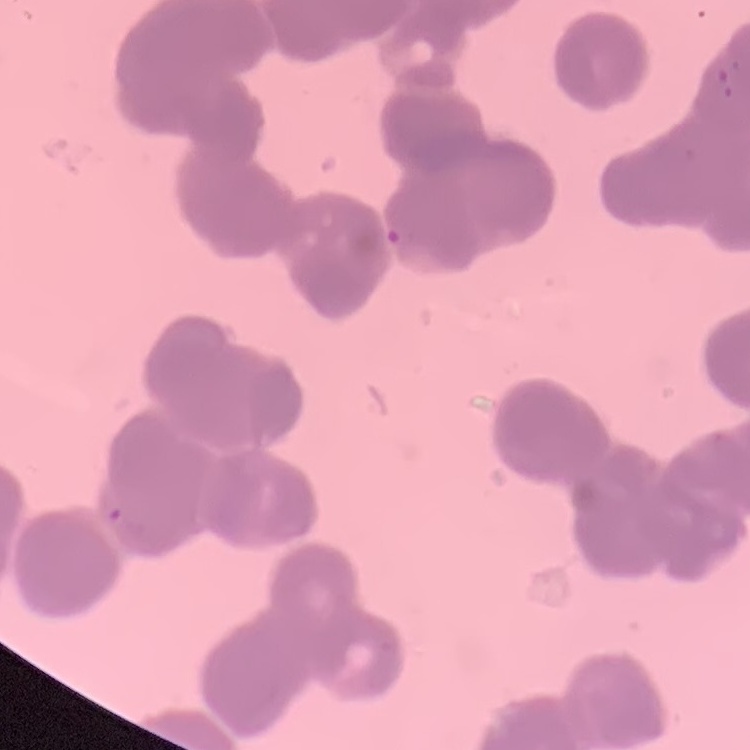
Summary:
  - Red blood cell morphology: rouleaux formation
  - Image type: square crop of a larger photomicrograph
  - Stain: Field's or Giemsa
  - Preparation: thin peripheral smear